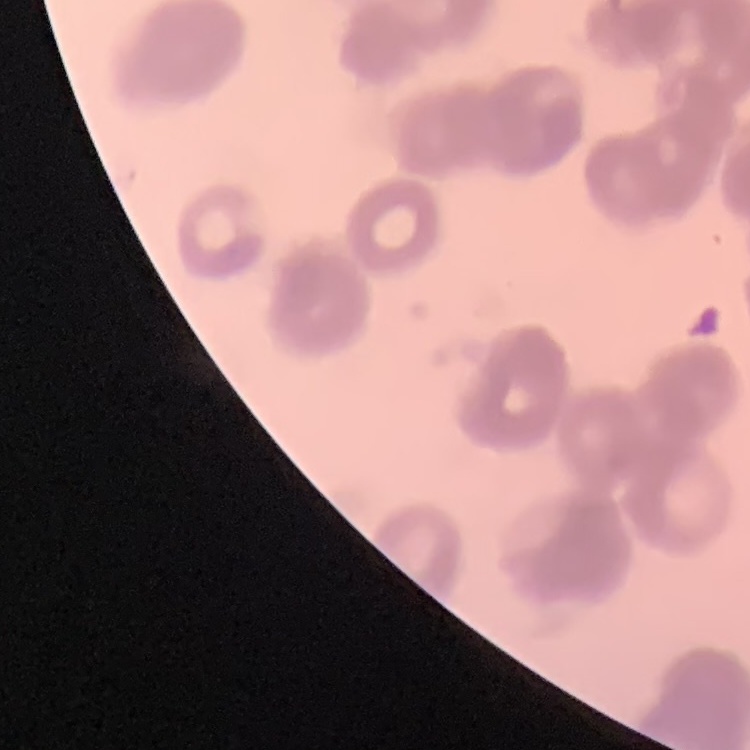

{
  "erythrocyte_morphology": "rouleaux formation",
  "preparation": "thin peripheral smear",
  "stain": "Field's or Giemsa",
  "image_type": "one tile cut from a larger photomicrograph"
}